Classify this cell by malaria status.
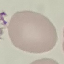

It is uninfected.

Summary:
  - Preparation: thin blood film
  - Image type: cell patch, automatically extracted from a larger field of view and resized to 64 × 64 pixels
  - Stain: Giemsa
  - Capture: smartphone through the microscope eyepiece